Assess for malaria.
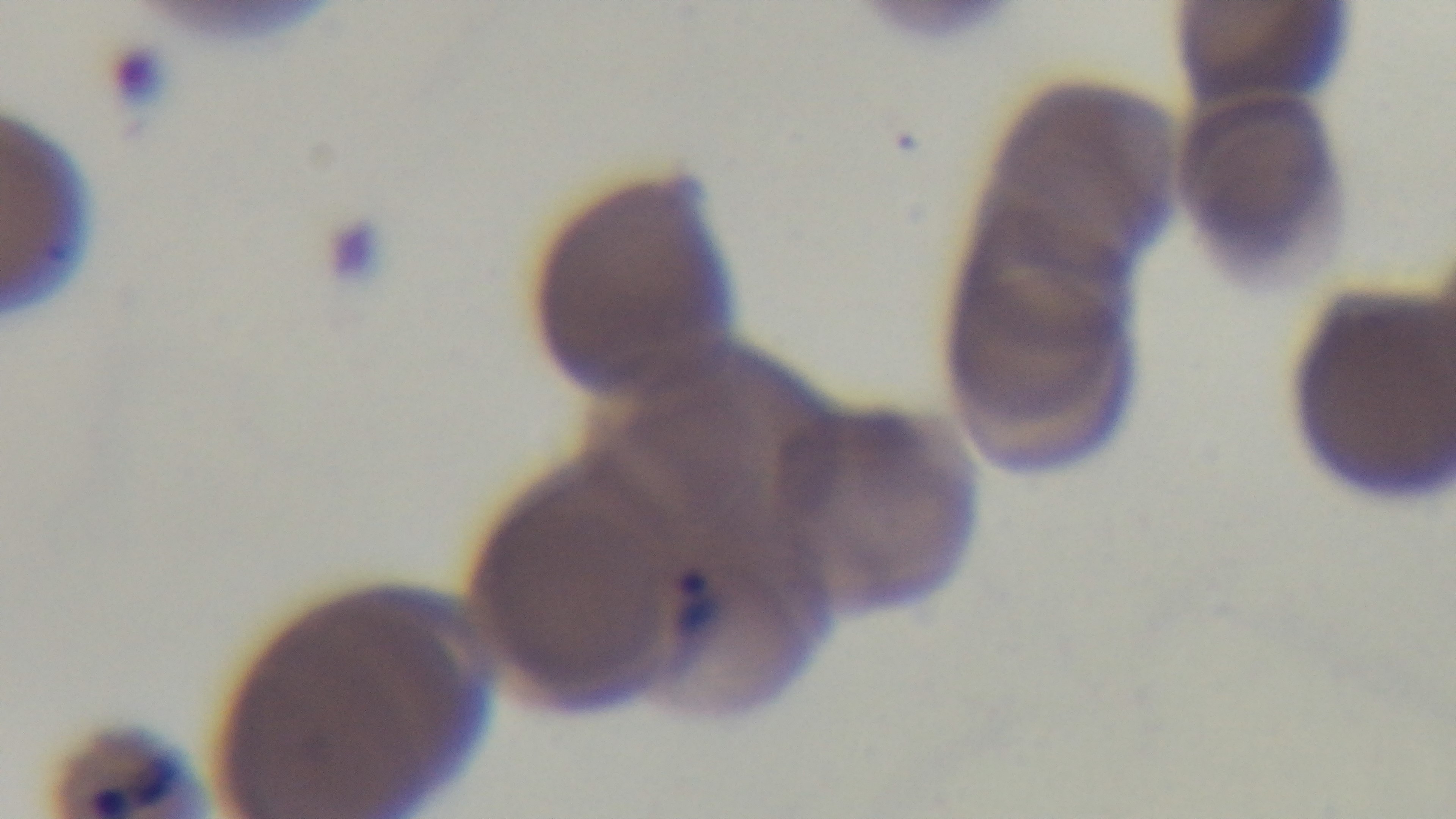
It is infected.

Summary:
  - Field of view: one from the slide
  - Capture: mounted 4K digital camera
  - Objective: 100x oil immersion
  - Modality: light microscopy
  - Stain: Giemsa
  - Preparation: thin blood film